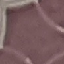
Summary:
  - Malaria status: uninfected
  - Capture: smartphone through the microscope eyepiece
  - Image type: cell patch, automatically extracted from a larger field of view and resized to 64 × 64 pixels
  - Stain: Giemsa
  - Preparation: thin blood film